Classify this cell by malaria status.
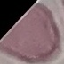
It is uninfected.

Giemsa stain. Thin blood smear. Photographed with a smartphone camera at the microscope eyepiece. Automatically extracted cell patch, resized to 64 × 64 pixels.